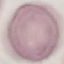

Summary:
  - Malaria status: uninfected
  - Image type: automatically extracted cell patch, resized to 64 × 64 pixels
  - Preparation: thin smear
  - Capture: smartphone through the microscope eyepiece
  - Stain: Giemsa